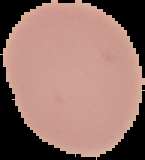

Summary:
  - Malaria status: uninfected
  - Preparation: thin blood film
  - Image type: segmented cell region with the area outside set to black
  - Image size: 145×160 pixels